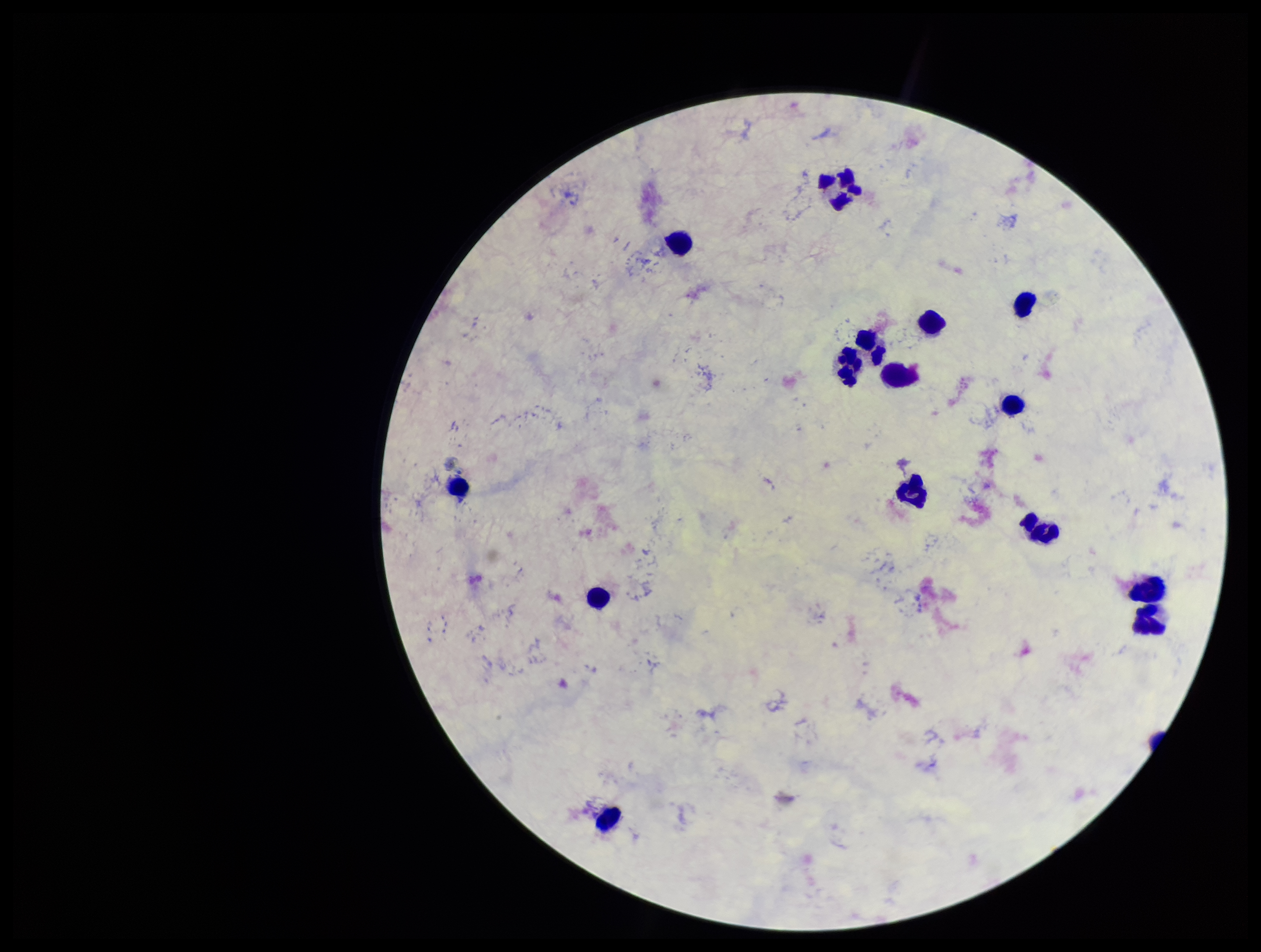
plasmodium_parasites: none detected
field_of_view: one from this slide
leukocyte_count: 15
capture: smartphone photograph through the microscope eyepiece
parasite_count: 0
patient_malaria_status: negative
preparation: thick blood smear
image_size: 1261×952 pixels
stain: Giemsa